Find each parasitized RBC.
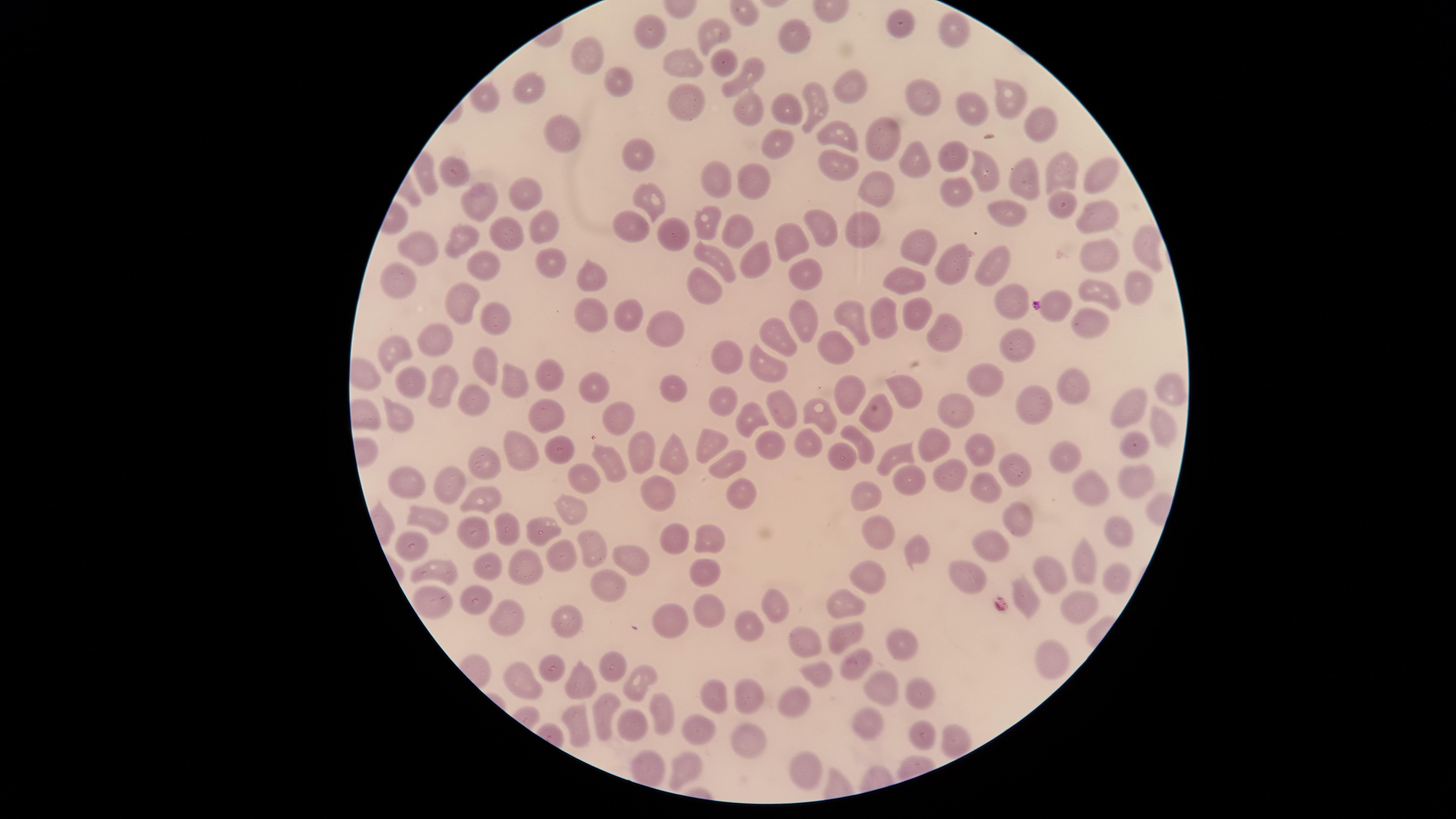
No parasitized RBCs identified.

Approximate marker points as {x, y} in pixels.
Summary:
  - Uninfected RBCs: {905, 24}, {649, 27}, {956, 27}, {714, 32}, {791, 34}, {587, 50}, {678, 56}, {721, 64}, {746, 74}, {614, 79}, {847, 87}, {536, 89}, {926, 94}, {1008, 96}, {493, 100}, {815, 102}, {681, 103}, {788, 104}, {743, 105}, {966, 107}, {1035, 119}, {562, 132}, {848, 132}, {883, 138}, {775, 143}, {632, 153}, {953, 153}, {915, 157}, {833, 161}, {978, 165}, {1055, 168}, {453, 169}, {1095, 171}, {714, 175}, {752, 176}, {1019, 176}, {950, 184}, {883, 185}, {530, 191}, {654, 199}, {480, 203}, {1007, 211}, {1059, 211}, {1101, 211}, {630, 218}, {536, 219}, {830, 219}, {707, 220}, {869, 222}, {744, 223}, {504, 231}, {666, 232}, {790, 233}, {1137, 236}, {462, 241}, {418, 244}, {912, 244}, {1094, 251}, {714, 255}, {957, 258}, {552, 259}, {755, 259}, {485, 265}, {807, 265}, {997, 265}, {909, 278}, {1133, 278}, {594, 279}, {399, 280}, {1100, 289}, {710, 290}, {1007, 299}, {1061, 299}, {461, 304}, {917, 307}, {627, 310}, {805, 311}, {883, 311}, {595, 314}, {494, 317}, {857, 317}, {665, 323}, {948, 323}, {1093, 324}, {775, 328}, {438, 339}, {1021, 340}, {838, 342}, {390, 348}, {726, 354}, {487, 363}, {771, 363}, {549, 371}, {986, 375}, {514, 377}, {446, 378}, {413, 381}, {1072, 384}, {589, 385}, {904, 386}, {1169, 387}, {674, 389}, {842, 393}, {471, 396}, {1023, 396}, {725, 403}, {786, 406}, {1128, 406}, {957, 408}, {744, 410}, {403, 412}, {546, 412}, {615, 412}, {818, 414}, {879, 419}, {1164, 422}, {711, 438}, {931, 440}, {769, 441}, {804, 441}, {862, 441}, {1130, 445}, {979, 446}, {515, 447}, {643, 450}, {672, 450}, {894, 452}, {562, 453}, {840, 453}, {1064, 455}, {1012, 459}, {727, 460}, {606, 462}, {486, 466}, {948, 471}, {582, 478}, {1132, 478}, {906, 480}, {404, 482}, {451, 482}, {979, 482}, {1088, 486}, {663, 491}, {871, 491}, {741, 493}, {479, 494}, {570, 510}, {434, 516}, {1021, 519}, {540, 523}, {509, 527}, {481, 529}, {1113, 530}, {875, 531}, {704, 537}, {668, 538}, {594, 539}, {993, 542}, {415, 543}, {561, 548}, {915, 548}, {1079, 556}, {636, 557}, {485, 561}, {440, 562}, {528, 563}, {705, 564}, {1052, 570}, {873, 571}, {1111, 575}, {970, 577}, {608, 589}, {1026, 591}, {427, 592}, {481, 598}, {850, 599}, {776, 604}, {1077, 606}, {714, 608}, {508, 612}, {681, 612}, {749, 622}, {564, 623}, {850, 628}, {804, 635}, {898, 645}, {1055, 656}, {551, 661}, {855, 661}, {610, 664}, {518, 671}, {814, 673}, {585, 680}, {637, 680}, {881, 685}, {714, 693}, {920, 695}, {748, 697}, {798, 700}, {608, 709}, {659, 711}, {575, 717}, {631, 724}, {874, 724}, {706, 733}, {920, 734}, {749, 739}, {951, 740}, {648, 760}, {685, 768}, {804, 768}
  - Field of view: single
  - Visible region: circular
  - Image size: 1456×819 pixels
  - Preparation: thin blood smear
  - Capture: smartphone photograph through the microscope eyepiece
  - Stain: Giemsa